Assess the morphology of the erythrocytes.
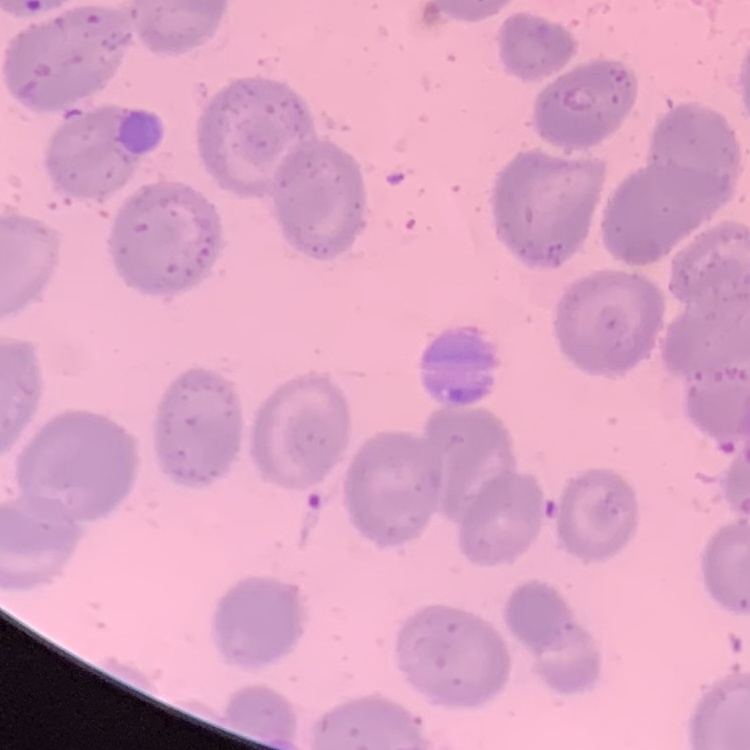

They show no rouleaux formation.

{
  "image_type": "one tile cut from a larger photomicrograph",
  "stain": "Field's or Giemsa",
  "preparation": "thin blood film"
}